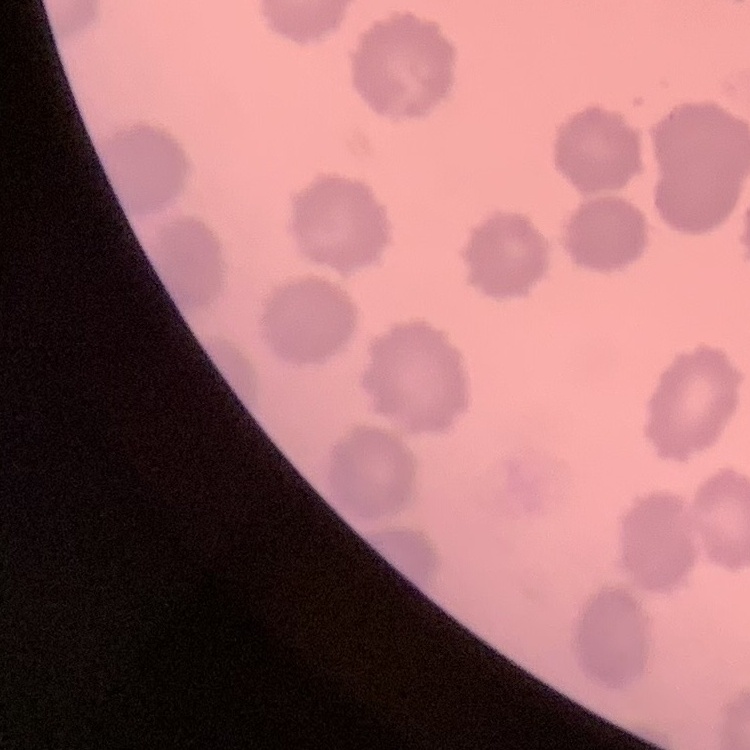
{
  "red_blood_cell_morphology": "no rouleaux formation",
  "stain": "Field's or Giemsa",
  "preparation": "thin peripheral smear",
  "image_type": "one tile cut from a larger photomicrograph"
}